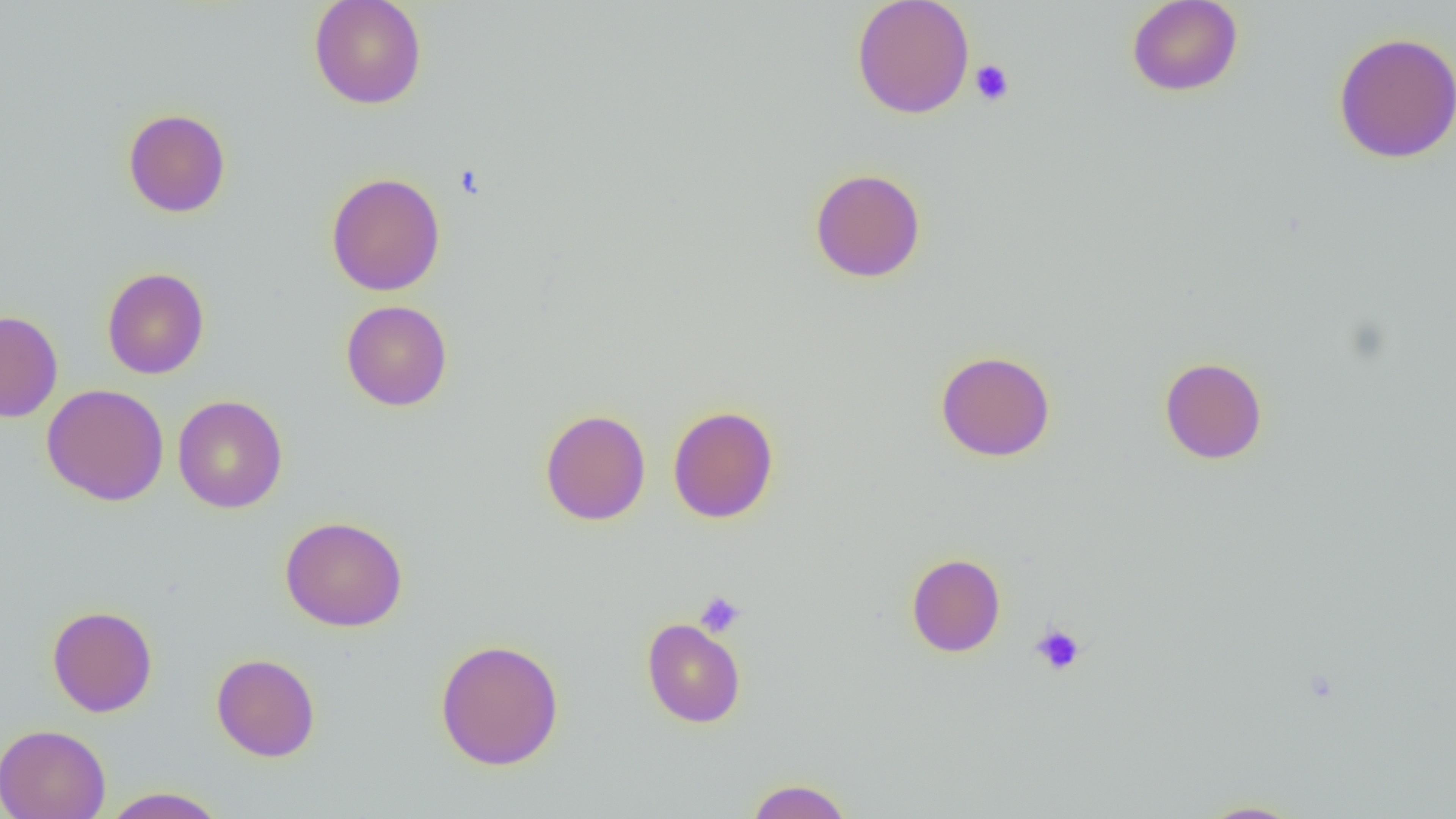
Approximate bounding boxes as (x1,y1)-(x2,y2) corner pairs in pixels. Platelet locations: (969,59)-(1015,106), (694,591)-(745,636), (1030,623)-(1086,675). Uninfected red blood cell locations: (309,0)-(427,109), (851,0)-(975,119), (1126,0)-(1244,97), (1333,32)-(1456,163), (123,108)-(231,217), (810,168)-(926,282), (326,172)-(445,296), (102,267)-(210,379), (341,300)-(452,411), (0,310)-(63,423), (935,350)-(1056,462), (1159,357)-(1267,464), (41,384)-(169,506), (172,395)-(288,514), (667,405)-(779,523), (539,409)-(651,526), (280,516)-(408,632), (906,553)-(1006,657), (47,605)-(158,717), (642,617)-(746,728), (435,639)-(564,770), (211,653)-(320,762), (0,724)-(111,819), (744,777)-(854,819), (100,786)-(229,818), (1195,799)-(1308,818). Slide-level diagnosis: no evidence of blood parasites. Optical microscopy. Thin blood smear. Image is 1456×819 pixels. Captured at 1000x magnification. One field of a larger specimen.